Describe the morphology of the red blood cells.
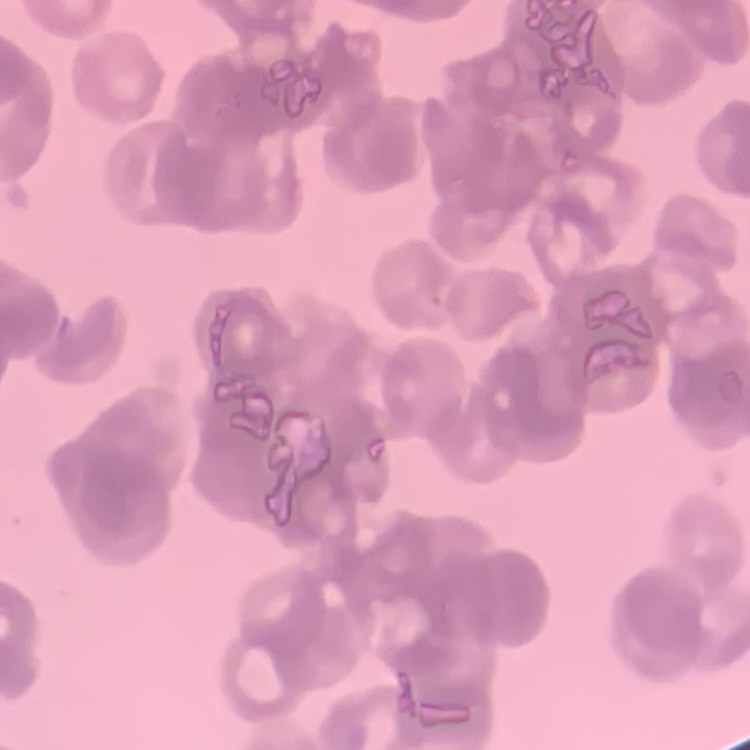
They show rouleaux formation.

Thin peripheral smear. One tile cut from a larger photomicrograph. Field's or Giemsa stain.